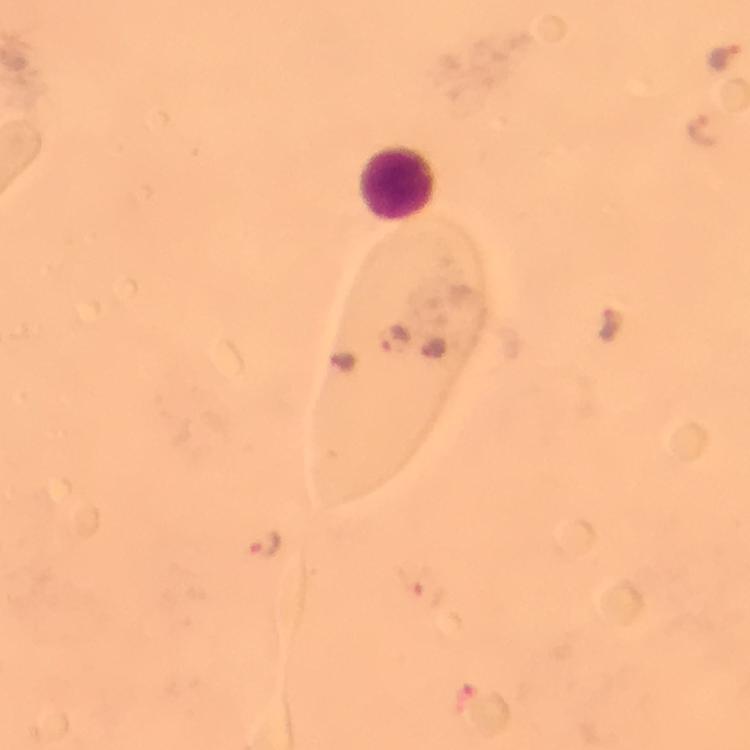
Approximate centers as (x, y) in pixels.
Summary:
  - Malaria parasite locations: (726, 56), (707, 130), (612, 324), (396, 339), (265, 543), (428, 594), (485, 712)
  - Leukocyte locations: (399, 183)
  - Image size: 750×750 pixels
  - Context: from a malaria diagnostic workup
  - Capture: smartphone mounted on the microscope
  - Preparation: thick blood film
  - Cropped from: one field of view
  - Immersion oil: applied
  - Stain: Giemsa
  - Magnification: 100x